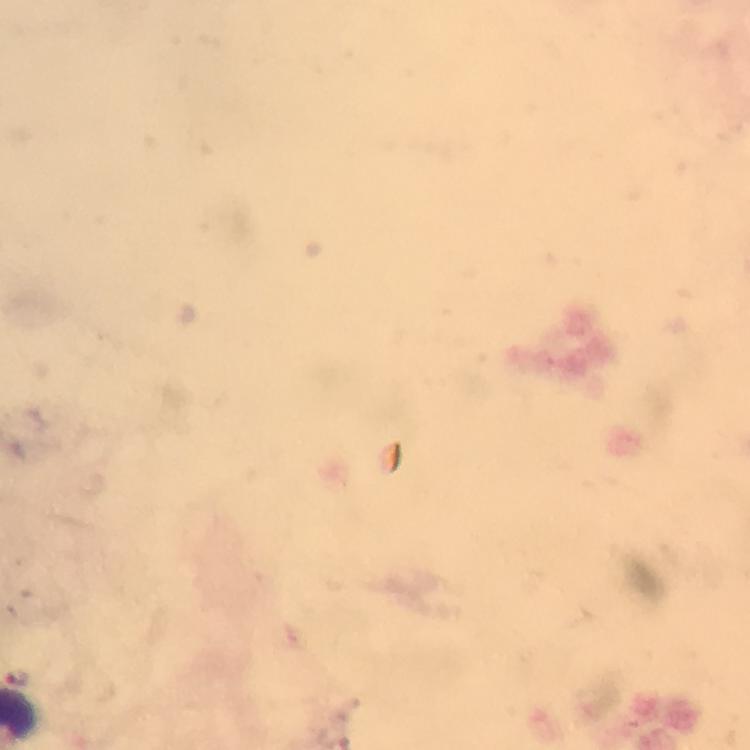
Approximate centers as [x, y] in pixels.
Summary:
  - Malaria parasite locations: [22, 678]
  - Magnification: 100x
  - Stain: Giemsa
  - Context: from a malaria diagnostic workup
  - Immersion oil: applied
  - Cropped from: one field of view
  - Image size: 750×750 pixels
  - Capture: smartphone photograph through a microscope
  - Preparation: thick smear